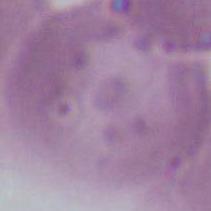

Summary:
  - Identification: red blood cell
  - Magnification: 1000x
  - Modality: micrograph